Identify the blood parasite species.
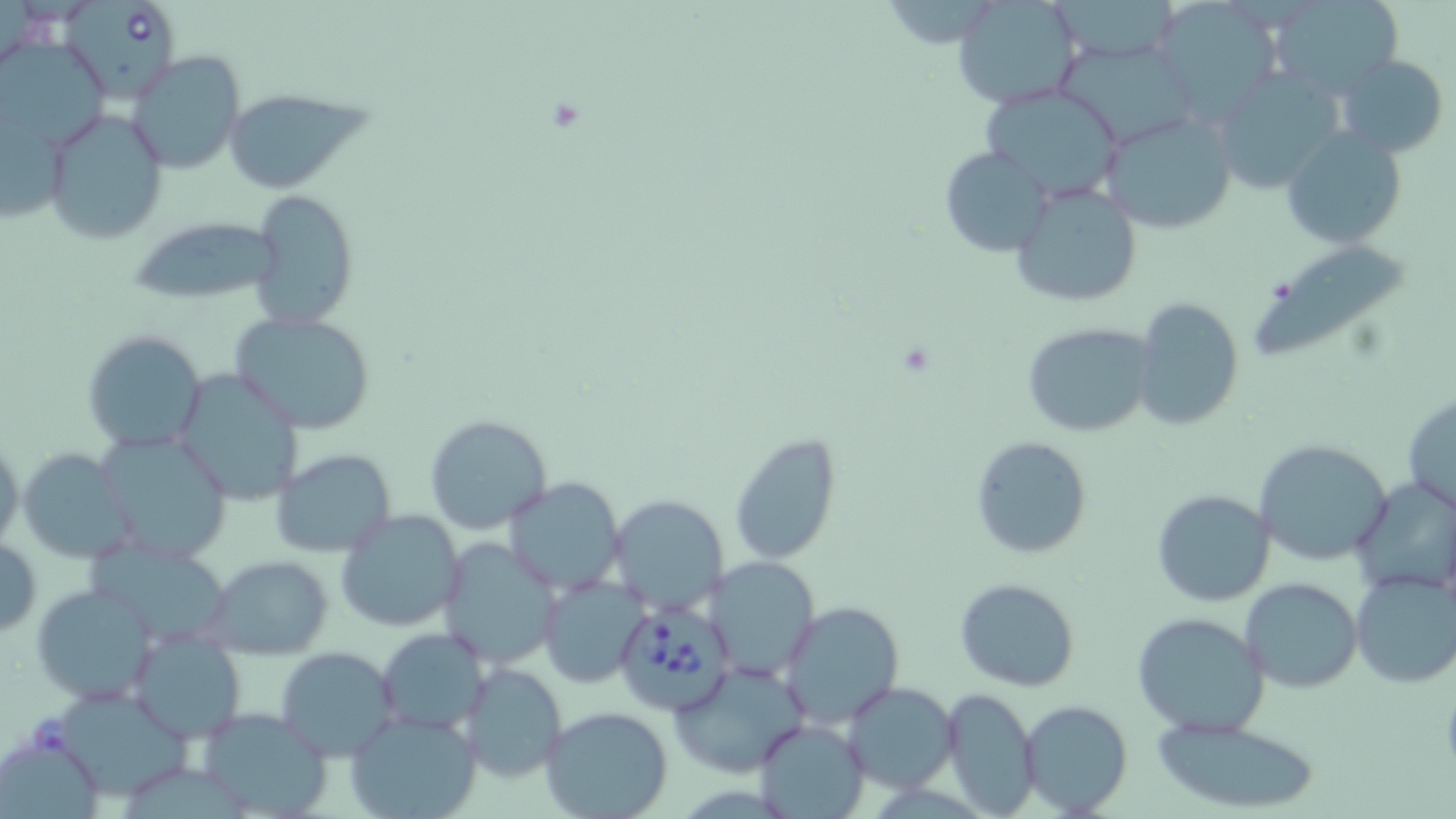

Babesia divergens.

{
  "field_of_view": "single",
  "platelet_locations": "approximate bounding boxes as (x1,y1)-(x2,y2) corner pairs in pixels: (543,95)-(589,135)",
  "preparation": "thin blood film",
  "modality": "optical microscopy",
  "image_size": "1456×819 pixels",
  "babesia_divergens_infected_red_blood_cell_locations": "approximate bounding boxes as (x1,y1)-(x2,y2) corner pairs in pixels: (61,0)-(182,103), (620,600)-(737,715)",
  "uninfected_red_blood_cell_locations": "approximate bounding boxes as (x1,y1)-(x2,y2) corner pairs in pixels: (951,0)-(1082,111), (1153,0)-(1284,122), (1265,0)-(1406,100), (1052,39)-(1199,148), (1,45)-(115,151), (126,51)-(246,174), (1336,53)-(1450,158), (1219,68)-(1353,195), (979,84)-(1125,200), (228,96)-(384,189), (42,107)-(168,244), (1098,109)-(1240,235), (1281,125)-(1406,248), (938,145)-(1055,257), (1009,178)-(1143,309), (248,190)-(361,331), (132,222)-(288,297), (1253,247)-(1405,357), (1130,296)-(1245,431), (231,312)-(377,434), (1021,322)-(1155,438), (81,329)-(207,454), (172,364)-(306,504), (1402,392)-(1456,516), (425,414)-(554,536), (94,428)-(233,564), (729,433)-(842,566), (0,434)-(24,559), (970,436)-(1093,558), (1252,438)-(1394,568), (16,446)-(144,564), (273,449)-(397,558), (1350,475)-(1456,596), (503,476)-(623,593), (1151,488)-(1276,606), (608,493)-(728,615), (335,509)-(465,633), (91,533)-(236,652), (0,534)-(41,640), (437,538)-(559,668), (203,555)-(334,658), (707,557)-(821,679), (1350,570)-(1455,688), (539,574)-(650,689), (1238,577)-(1363,693), (954,578)-(1080,692), (32,581)-(158,705), (783,603)-(901,728), (1132,612)-(1271,737), (377,628)-(488,735), (130,629)-(245,742), (275,647)-(400,761), (668,661)-(810,778), (461,662)-(567,781), (844,681)-(959,793), (465,683)-(670,798), (942,687)-(1039,816), (56,692)-(196,800), (1018,699)-(1133,816), (197,705)-(333,818), (540,707)-(674,819), (345,709)-(482,819), (1143,713)-(1330,814), (754,718)-(868,817), (3,738)-(104,818)",
  "magnification": "1000x",
  "stain": "May-Grünwald-Giemsa"
}